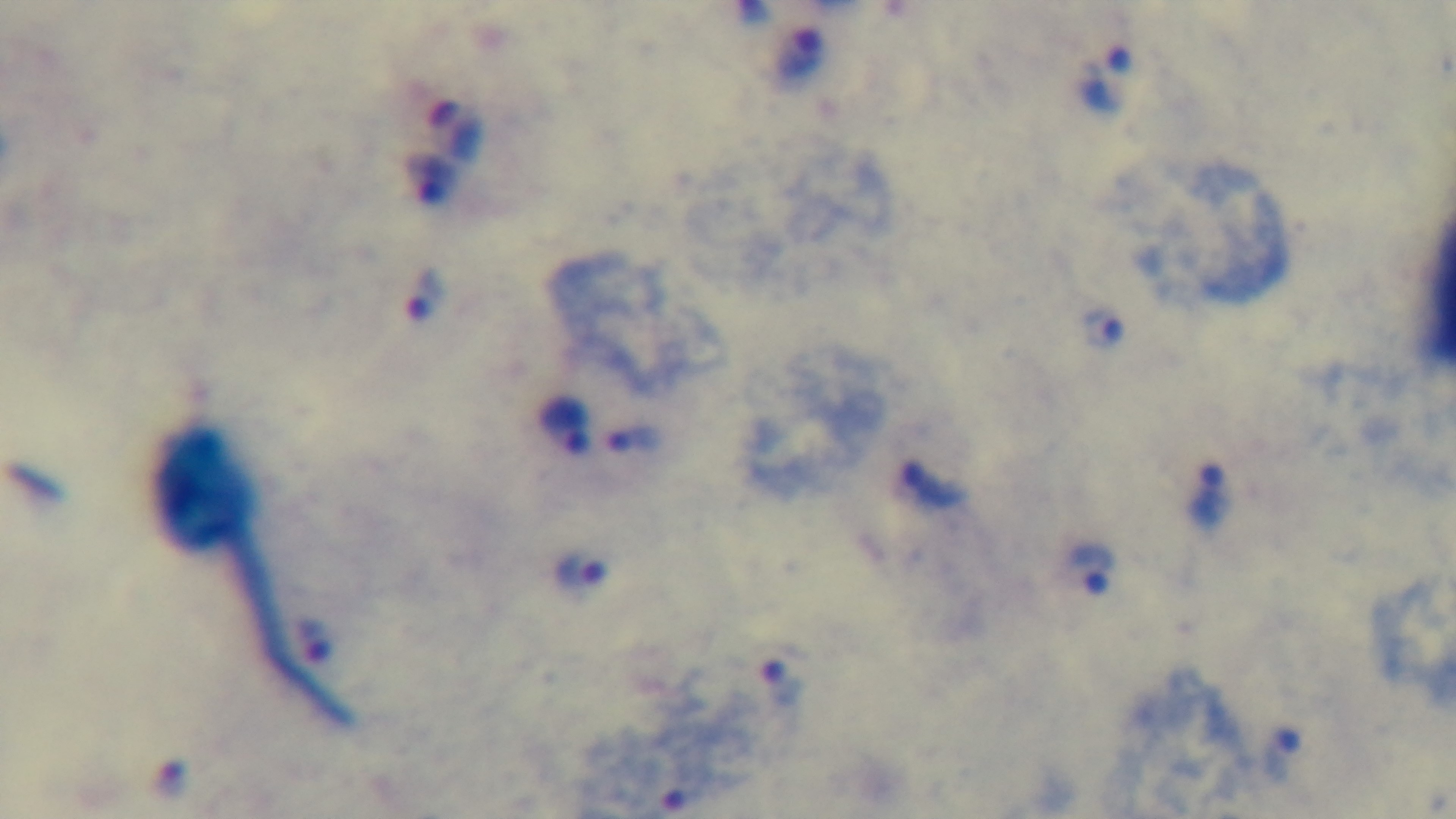

100x oil-immersion objective. Malaria status: infected. Preparation: thick blood film. Captured with a mounted 4K digital camera. Light microscopy. Giemsa stain. One field from the slide.